Outline each blood parasite and name the species.
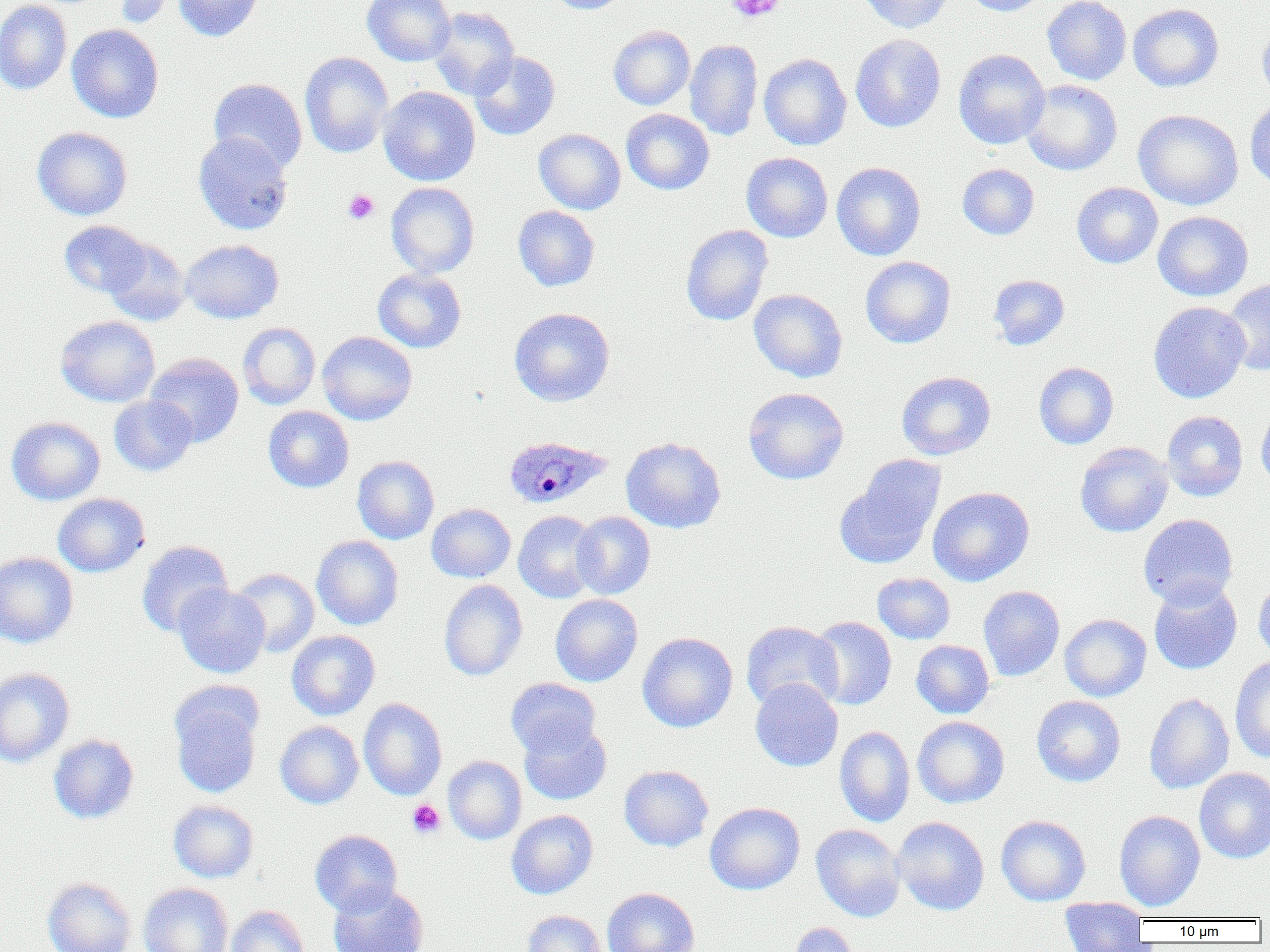

Approximate bounding boxes as [x1, y1, x2, y2] in pixels.
Plasmodium ovale-infected red blood cells: [503, 436, 612, 509].
No Plasmodium falciparum, Plasmodium malariae, Plasmodium vivax, Babesia divergens, or Trypanosoma brucei observed.

{
  "slide_level_diagnosis": "Plasmodium ovale",
  "image_size": "1270×952 pixels",
  "platelet_locations": "approximate bounding boxes as [x1, y1, x2, y2] in pixels: [725, 0, 785, 23], [343, 189, 379, 224], [407, 799, 445, 838]",
  "field_of_view": "single",
  "preparation": "thin blood film",
  "magnification": "1000x",
  "modality": "optical microscopy",
  "uninfected_red_blood_cell_locations": "approximate bounding boxes as [x1, y1, x2, y2] in pixels: [0, 0, 72, 94], [114, 0, 178, 27], [174, 0, 265, 41], [362, 0, 456, 66], [542, 0, 630, 14], [858, 0, 954, 33], [961, 0, 1049, 16], [1042, 0, 1132, 85], [1128, 3, 1224, 92], [429, 6, 519, 99], [1257, 21, 1270, 105], [67, 24, 163, 123], [608, 25, 695, 110], [850, 34, 946, 132], [685, 39, 763, 140], [953, 49, 1050, 149], [299, 51, 393, 158], [469, 51, 560, 140], [759, 53, 851, 150], [209, 78, 307, 173], [1021, 80, 1122, 175], [377, 86, 480, 186], [1245, 97, 1270, 191], [621, 109, 714, 195], [1133, 109, 1244, 210], [32, 127, 133, 220], [534, 128, 626, 214], [193, 132, 293, 235], [741, 152, 833, 242], [831, 162, 926, 260], [957, 163, 1039, 240], [386, 182, 479, 278], [1072, 182, 1163, 268], [513, 206, 599, 291], [1153, 211, 1253, 301], [60, 221, 150, 298], [681, 224, 773, 326], [102, 237, 191, 326], [180, 239, 283, 323], [860, 256, 956, 348], [373, 268, 466, 353], [988, 274, 1070, 350], [1221, 279, 1270, 375], [749, 289, 847, 383], [1148, 301, 1251, 403], [510, 307, 615, 407], [56, 316, 160, 407], [237, 322, 320, 409], [317, 331, 417, 425], [145, 352, 244, 447], [1034, 362, 1119, 449], [896, 371, 996, 460], [743, 387, 849, 485], [109, 396, 197, 476], [1256, 403, 1270, 492], [263, 406, 354, 492], [1162, 411, 1248, 501], [6, 416, 104, 505], [621, 436, 726, 533], [1075, 442, 1173, 537], [352, 455, 439, 544], [835, 457, 945, 569], [927, 486, 1034, 586], [52, 493, 150, 577], [426, 503, 515, 582], [513, 510, 601, 603], [570, 511, 655, 599], [1138, 514, 1238, 609], [312, 535, 404, 630], [135, 540, 234, 636], [0, 552, 78, 648], [230, 567, 320, 657], [872, 573, 955, 644], [1253, 575, 1270, 665], [439, 579, 528, 681], [1148, 581, 1242, 674], [173, 583, 270, 678], [978, 586, 1065, 681], [550, 594, 643, 686], [1059, 613, 1151, 701], [808, 616, 896, 710], [741, 620, 842, 712], [286, 630, 380, 720], [637, 632, 738, 732], [911, 639, 995, 718], [1230, 657, 1270, 763], [0, 668, 74, 767], [506, 678, 601, 758], [750, 678, 843, 772], [168, 686, 263, 798], [1144, 693, 1234, 794], [1031, 695, 1125, 787], [358, 698, 447, 800], [912, 716, 1009, 808], [519, 720, 612, 805], [275, 721, 363, 809], [834, 725, 915, 827], [49, 734, 139, 823], [443, 755, 527, 844], [618, 765, 713, 851], [1194, 767, 1270, 863], [168, 800, 259, 883], [705, 802, 805, 895], [506, 810, 599, 899], [1114, 810, 1206, 911], [996, 815, 1091, 905], [891, 816, 990, 915], [811, 824, 906, 922], [310, 829, 402, 916], [42, 877, 136, 952], [327, 882, 428, 952], [138, 883, 233, 952], [601, 887, 699, 952], [1059, 897, 1150, 950], [226, 905, 311, 952], [521, 910, 608, 952], [789, 922, 859, 952]"
}